Name the parasite shown.
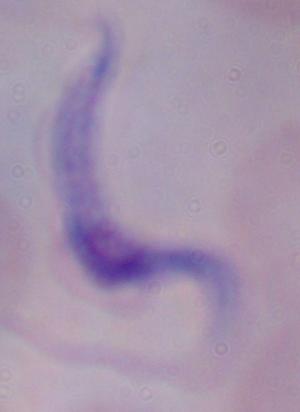
This is a trypanosome.

magnification = 1000x
modality = photomicrograph